Classify this cell by malaria status.
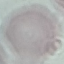
It is uninfected.

Summary:
  - Stain: Giemsa
  - Preparation: thin blood film
  - Capture: smartphone camera at the microscope eyepiece
  - Image type: automatically extracted cell patch, resized to 64 × 64 pixels